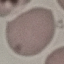 Result: no malaria parasites seen. Acquired by smartphone through the microscope eyepiece. Thin smear of blood. Cell patch, automatically extracted from a larger field of view and resized to 64 × 64 pixels. Giemsa-stained preparation.